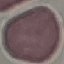
Summary:
  - Result: no malaria parasites seen
  - Preparation: thin smear
  - Capture: smartphone through the microscope eyepiece
  - Image type: automatically extracted cell patch, resized to 64 × 64 pixels
  - Stain: Giemsa